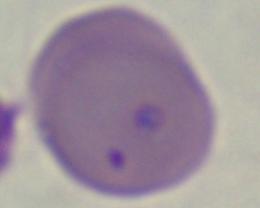

identification: Babesia
magnification: 1000x
modality: micrograph